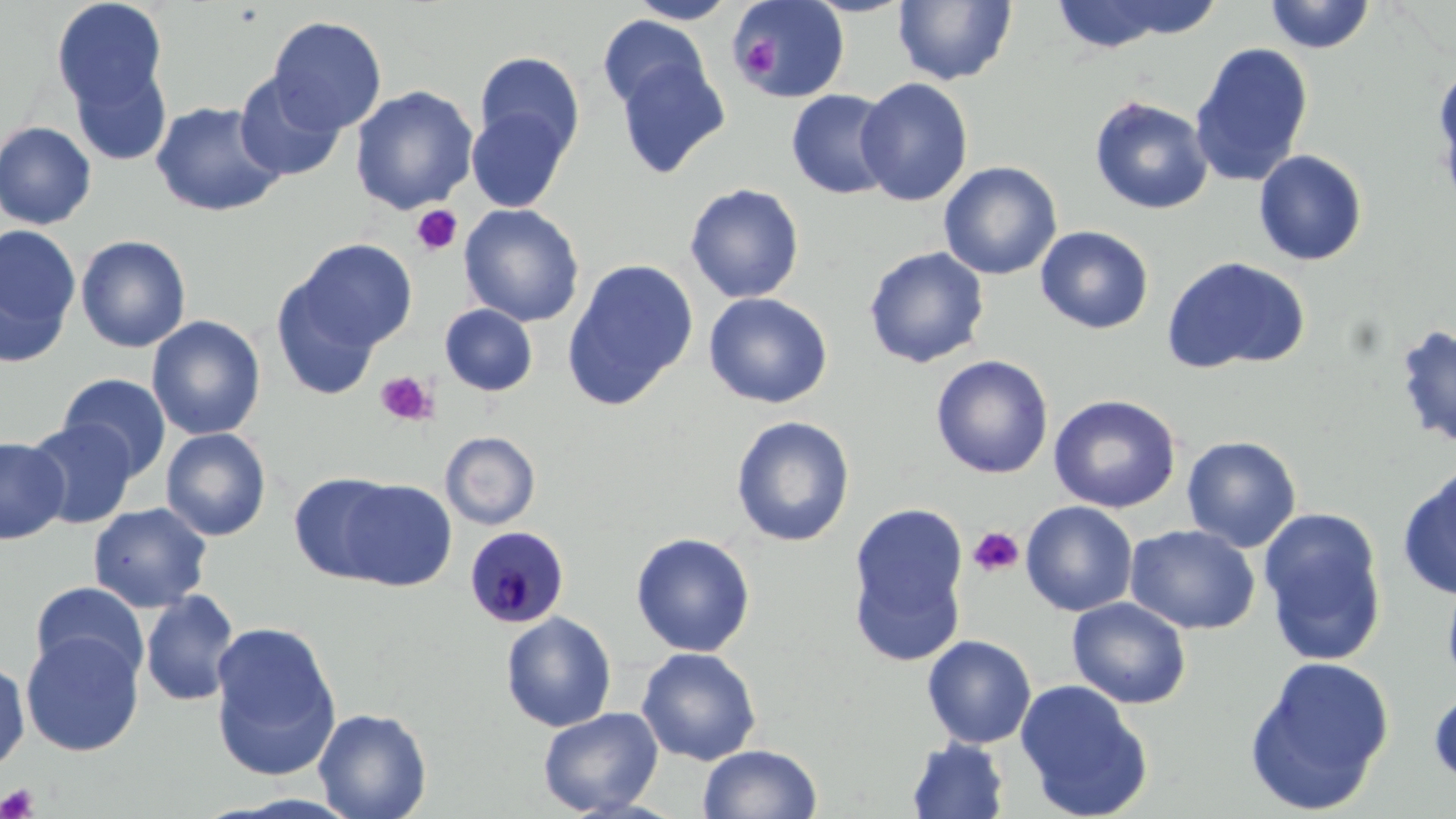
slide-level diagnosis = Plasmodium malariae
modality = light microscopy
uninfected red blood cell locations = approximate bounding boxes as [x1, y1, x2, y2] in pixels: [51, 0, 169, 118], [732, 0, 850, 103], [1047, 0, 1185, 54], [1092, 0, 1228, 41], [625, 1, 739, 24], [892, 1, 1018, 86], [1264, 1, 1376, 54], [267, 15, 387, 135], [598, 15, 710, 114], [1189, 42, 1313, 187], [474, 51, 585, 161], [612, 54, 731, 180], [67, 57, 173, 168], [1433, 62, 1456, 209], [234, 72, 347, 182], [855, 78, 974, 206], [349, 85, 479, 214], [785, 89, 897, 200], [1089, 96, 1213, 215], [150, 100, 286, 218], [465, 105, 572, 213], [0, 121, 98, 230], [1253, 149, 1368, 266], [938, 161, 1062, 280], [684, 183, 805, 304], [458, 203, 585, 327], [0, 225, 81, 365], [1035, 225, 1154, 334], [75, 235, 191, 353], [288, 238, 418, 358], [863, 246, 990, 369], [1161, 255, 1311, 375], [562, 259, 699, 410], [270, 273, 386, 401], [703, 292, 833, 409], [438, 303, 538, 397], [147, 316, 266, 441], [1392, 323, 1456, 451], [930, 354, 1054, 479], [57, 373, 172, 480], [1047, 394, 1181, 514], [731, 415, 855, 547], [25, 419, 138, 529], [161, 427, 272, 541], [440, 431, 541, 530], [1181, 435, 1302, 552], [0, 436, 70, 545], [1398, 465, 1456, 601], [288, 472, 405, 583], [332, 477, 457, 591], [1020, 500, 1138, 617], [88, 503, 212, 613], [846, 503, 970, 665], [1257, 506, 1388, 665], [1126, 524, 1260, 635], [630, 532, 756, 657], [1441, 574, 1456, 697], [29, 581, 150, 684], [139, 589, 241, 707], [1066, 597, 1192, 710], [500, 611, 617, 732], [208, 619, 342, 782], [20, 630, 144, 757], [921, 635, 1037, 749], [636, 646, 762, 765], [1244, 656, 1395, 814], [0, 659, 30, 774], [1014, 679, 1153, 819], [1429, 686, 1456, 788], [313, 707, 433, 819], [538, 707, 663, 817], [907, 739, 1009, 819], [698, 743, 823, 819]
stain = May-Grünwald-Giemsa
platelet locations = approximate bounding boxes as [x1, y1, x2, y2] in pixels: [736, 38, 780, 81], [410, 204, 464, 256], [374, 369, 438, 428], [966, 527, 1024, 578], [0, 783, 40, 818]
preparation = thin blood smear
field of view = one of a larger specimen
magnification = 1000x
image size = 1456×819 pixels
Plasmodium malariae-infected red blood cell locations = approximate bounding boxes as [x1, y1, x2, y2] in pixels: [462, 525, 570, 629]